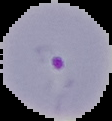

Summary:
  - Image type: segmented cell region with the area outside set to black
  - Preparation: thin blood film
  - Image size: 112×121 pixels
  - Result: Plasmodium parasites identified